Locate every malaria parasite and every leukocyte.
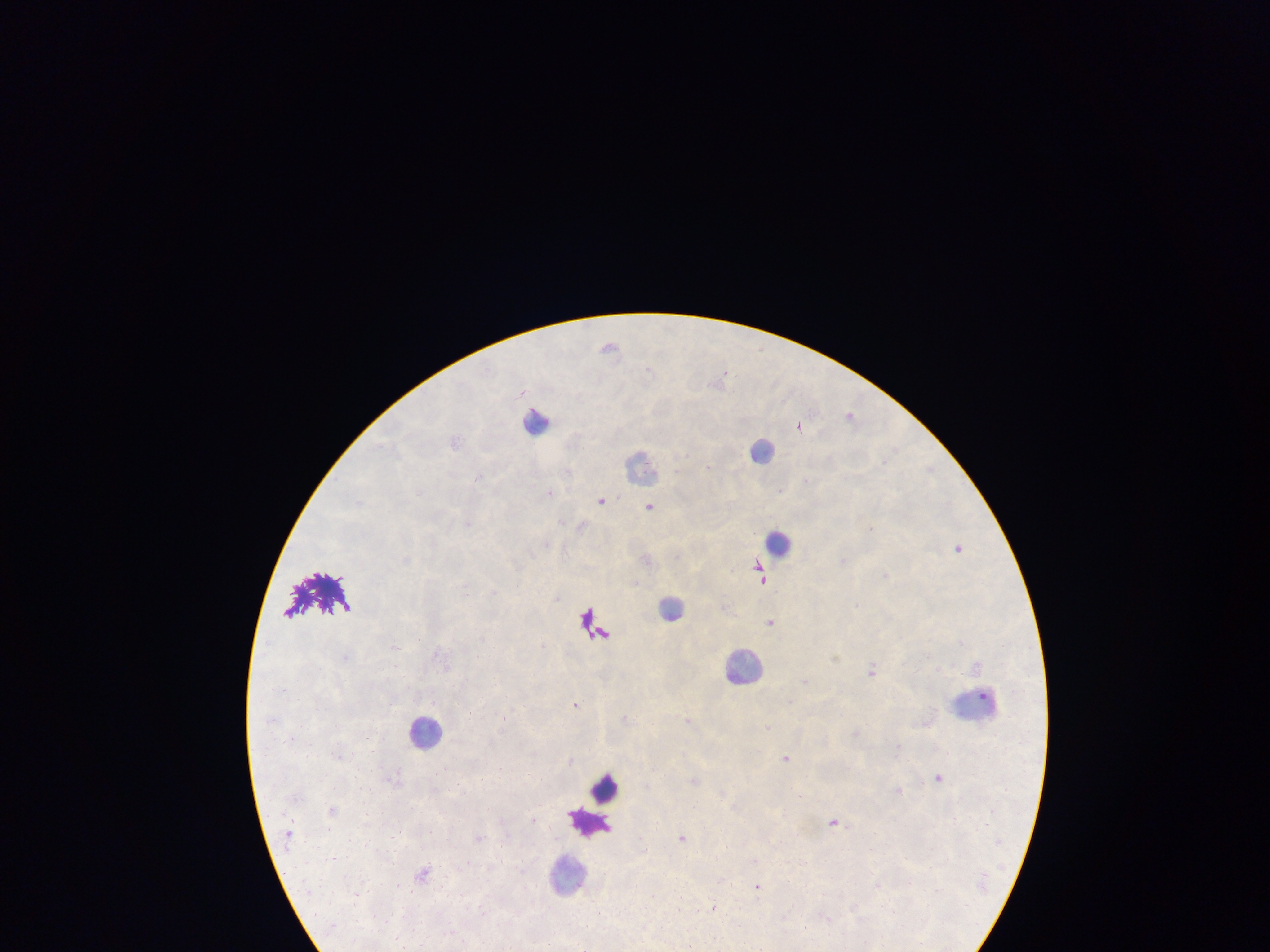
Approximate centers as [x, y] in pixels.
Malaria parasites: [609, 345], [725, 372], [850, 414], [799, 426], [709, 466], [479, 476], [550, 492], [602, 500], [358, 502], [650, 506], [467, 523], [959, 548], [844, 560], [762, 578], [770, 621], [346, 657], [872, 670], [805, 681], [575, 704], [689, 720], [768, 727], [856, 732], [786, 758], [571, 759], [500, 768], [939, 777], [695, 780], [898, 790], [835, 822], [396, 835], [478, 836], [682, 837], [757, 885], [713, 907], [483, 912].
Leukocytes: [538, 422], [763, 450], [641, 466], [779, 543], [672, 607], [744, 665], [975, 708], [427, 731], [606, 790], [587, 822], [567, 874].

preparation = thick blood film
field of view = single
country = Ghana
capture = mobile-phone photograph through a microscope
image size = 1270×952 pixels